Name the parasite shown.
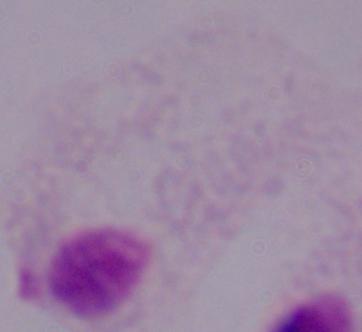

This is a trichomonad.

Captured at 1000x magnification. Photomicrograph.